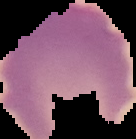
preparation = thin blood smear
image type = segmented cell region with the area outside set to black
image size = 136×139 pixels
malaria status = uninfected